Assess the morphology of the red blood cells.
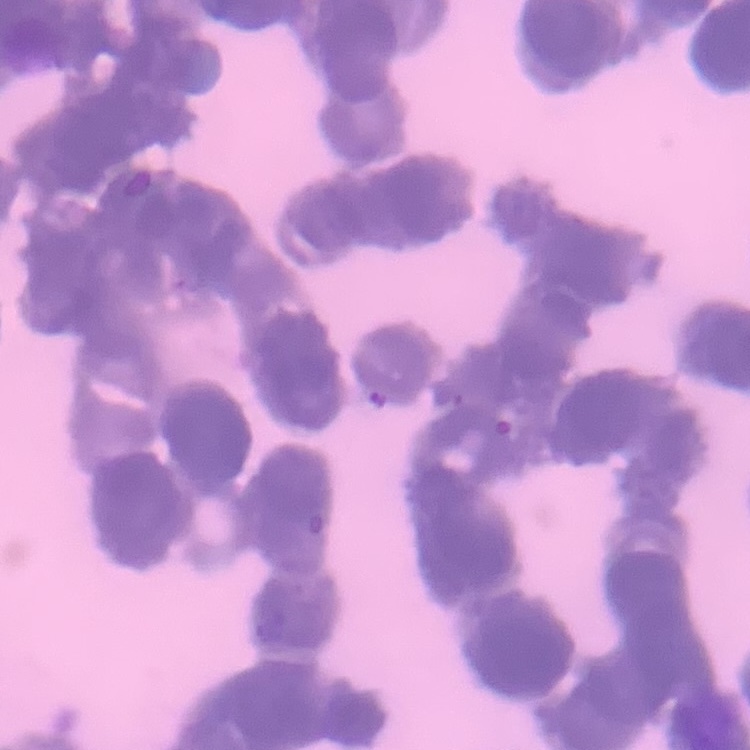

They show rouleaux formation.

Field's or Giemsa stain. Square crop of a larger photomicrograph. Thin blood smear.